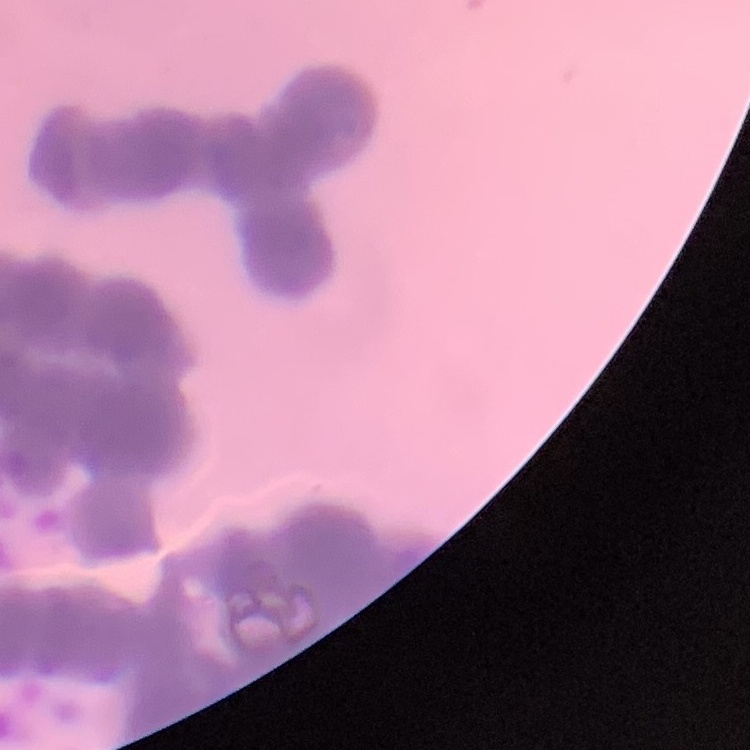
erythrocyte morphology = rouleaux formation
preparation = thin blood film
image type = square crop of a larger photomicrograph
stain = Field's or Giemsa